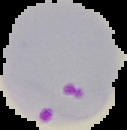
{
  "image_size": "127×130 pixels",
  "image_type": "segmented cell region with the area outside set to black",
  "result": "malaria parasites identified",
  "preparation": "thin blood smear"
}